Identify the parasite.
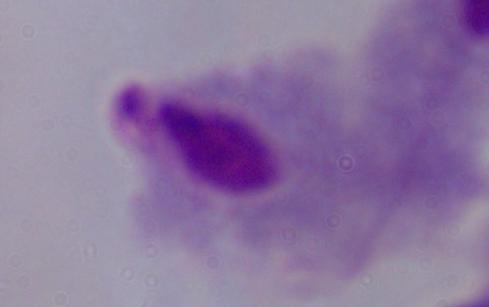

A trichomonad.

Summary:
  - Modality: photomicrograph
  - Magnification: 1000x